Describe the morphology of the red blood cells.
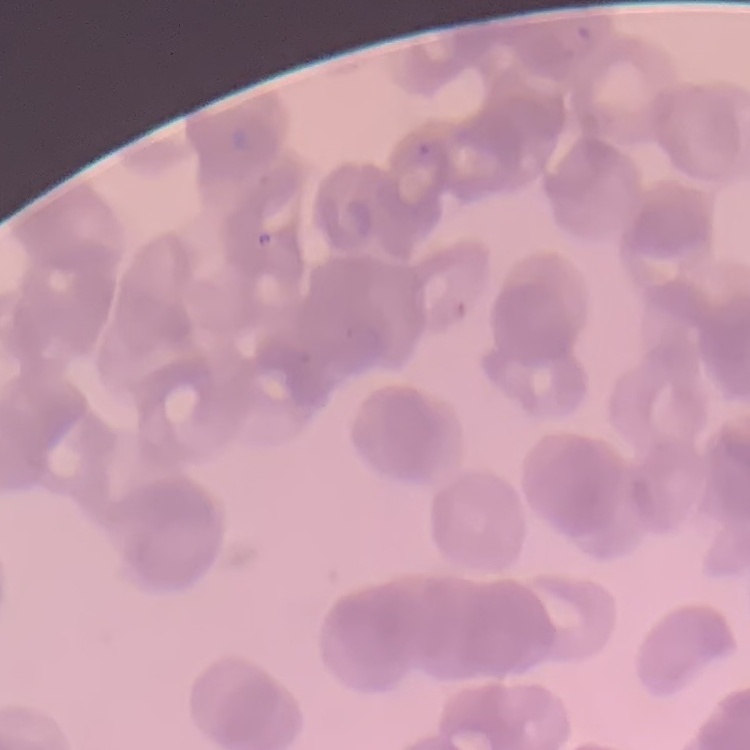
They show rouleaux formation.

One tile cut from a larger photomicrograph. Field's or Giemsa stain. Thin blood smear.